Assess the morphology of the red blood cells.
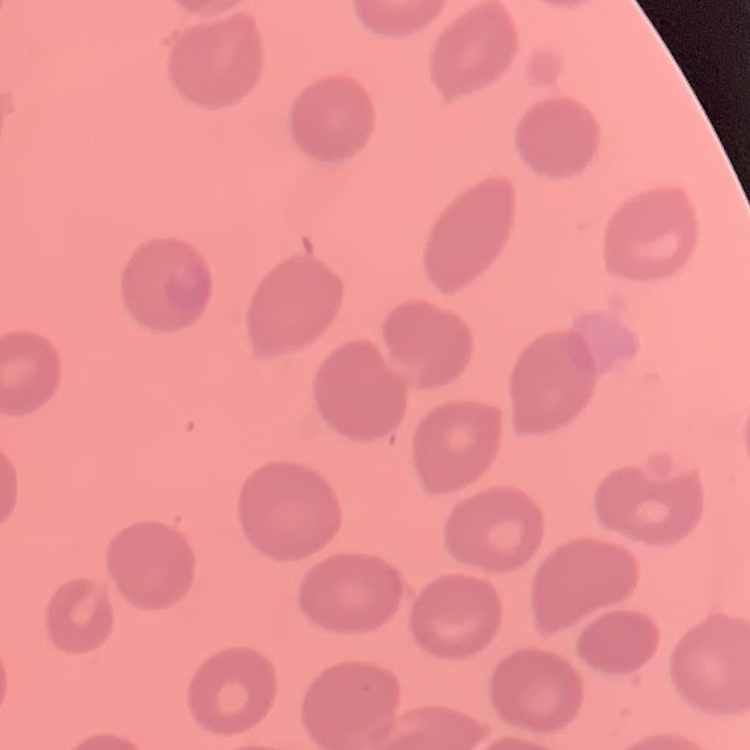
No rouleaux formation.

Summary:
  - Image type: one tile cut from a larger photomicrograph
  - Stain: Field's or Giemsa
  - Preparation: thin blood film